Assess this cell for malaria.
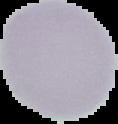
It is uninfected.

The area outside the segmented cell region is set to black. From a thin blood film. Image is 118×124 pixels.